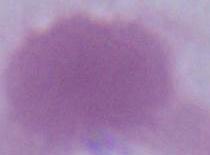

identification = erythrocyte
magnification = 1000x
modality = micrograph